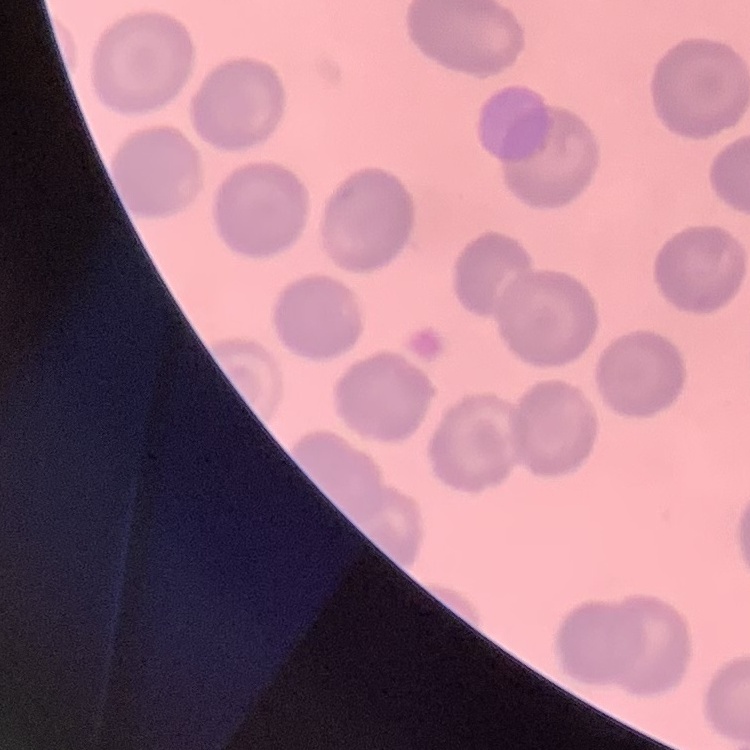

Summary:
  - Red blood cell morphology: no rouleaux formation
  - Stain: Field's or Giemsa
  - Preparation: thin peripheral smear
  - Image type: square crop of a larger photomicrograph